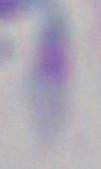
Summary:
  - Identification: Toxoplasma gondii
  - Magnification: 1000x
  - Modality: photomicrograph